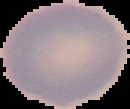 The area outside the segmented cell region is set to black. From a thin blood film. Image is 130×109 pixels. Malaria status: uninfected.